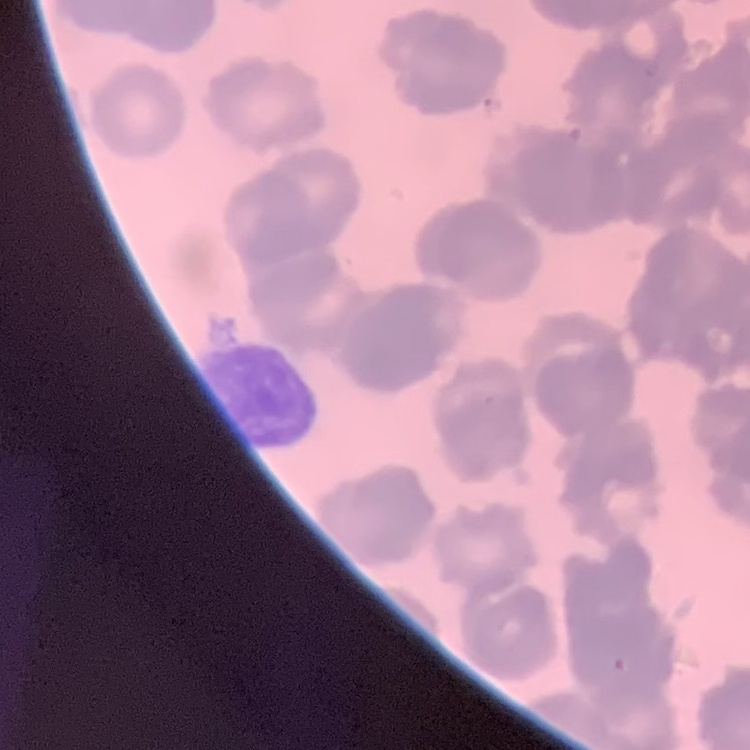

Summary:
  - Red blood cell morphology: rouleaux formation
  - Preparation: thin peripheral smear
  - Image type: square crop of a larger photomicrograph
  - Stain: Field's or Giemsa